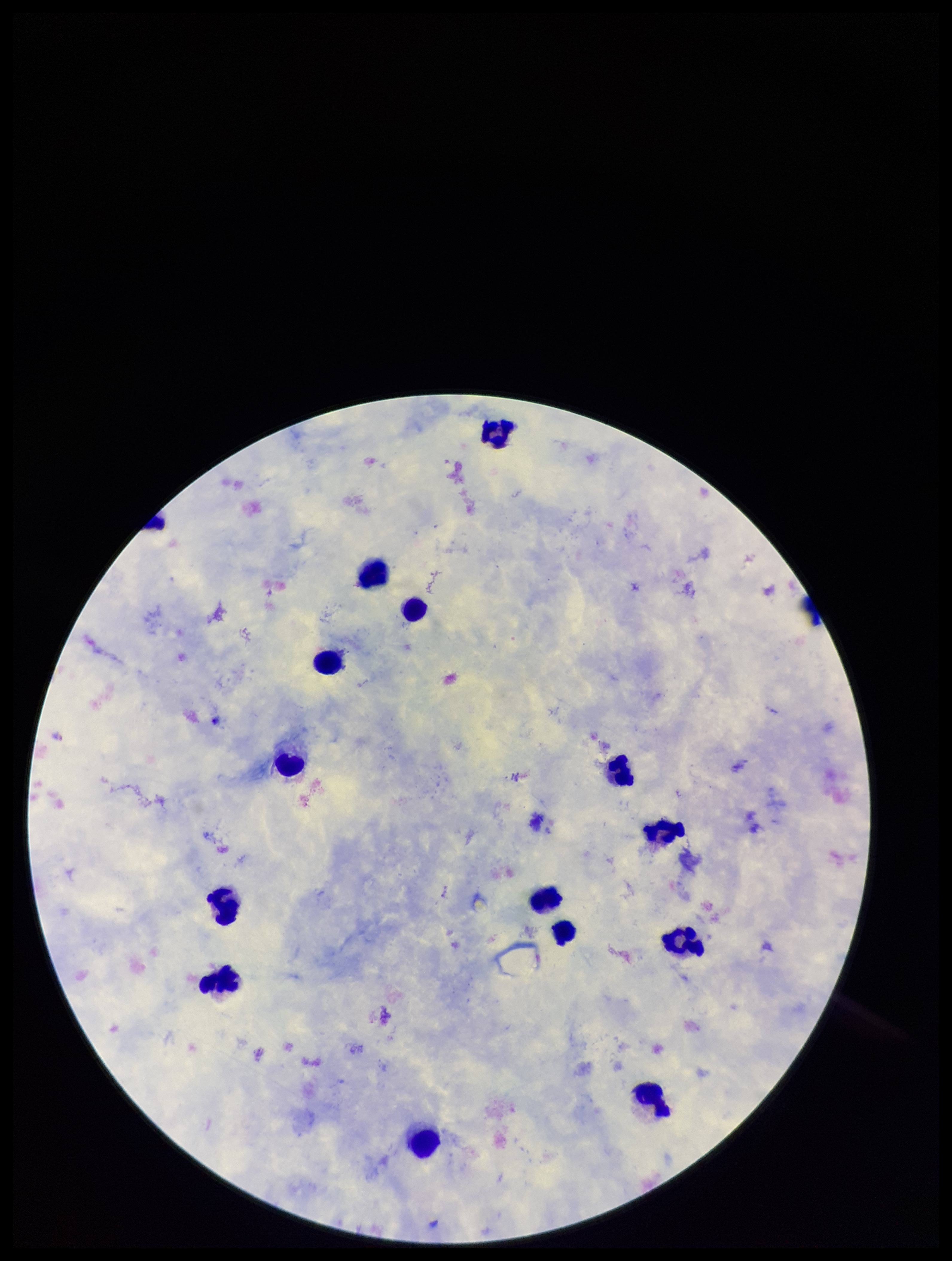
Stained with Giemsa. One field from this slide. Species reported for this patient: Plasmodium falciparum. Preparation: thick. Patient malaria status: positive. Image is 952×1261 pixels. Parasite count: 0. Plasmodium parasites: none detected. Leukocyte count: 14. Smartphone photograph taken through the eyepiece of a microscope.